Classify this cell by malaria status.
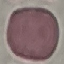
It is uninfected.

stain = Giemsa
capture = smartphone camera at the microscope eyepiece
image type = automatically extracted cell patch, resized to 64 × 64 pixels
preparation = thin blood smear